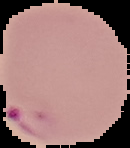

{
  "image_type": "cell region segmented out of the field of view; surrounding area masked to black",
  "preparation": "thin blood film",
  "malaria_status": "parasitized",
  "image_size": "130×148 pixels"
}